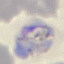 Malaria status: parasitized. Giemsa-stained preparation. Acquired by smartphone through the microscope eyepiece. Thin blood film. Automatically extracted cell patch, resized to 64 × 64 pixels.